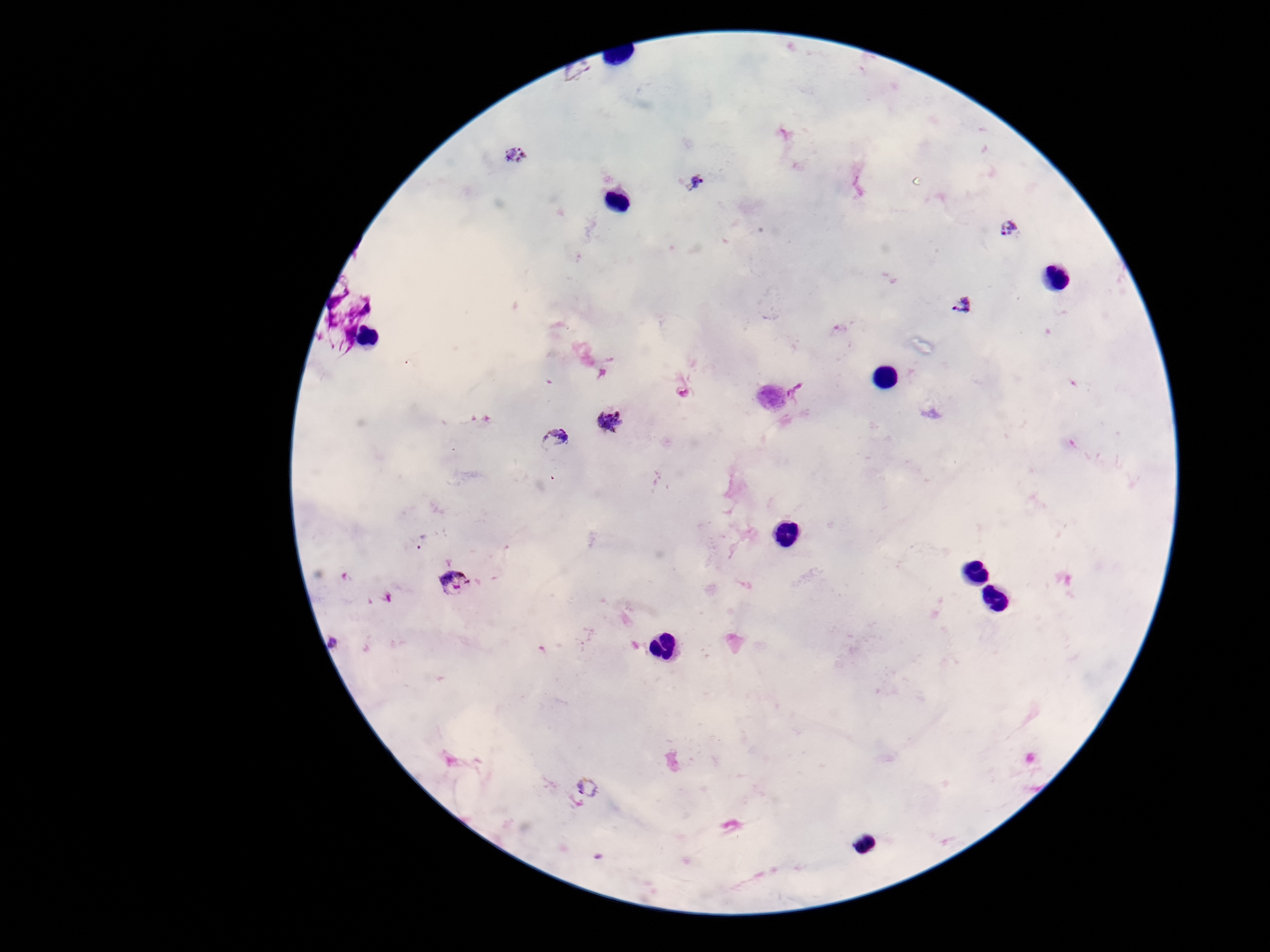
preparation = thick peripheral-blood smear
image size = 1270×952 pixels
magnification = 100x
field of view = single
capture = smartphone camera through the microscope eyepiece
Plasmodium parasite locations = approximate centers as {x, y} in pixels: {580, 72}, {514, 156}, {695, 182}, {1009, 228}, {962, 307}, {798, 393}, {609, 422}, {556, 438}, {455, 582}, {337, 643}, {586, 788}
stain = Giemsa
patient malaria status = infected